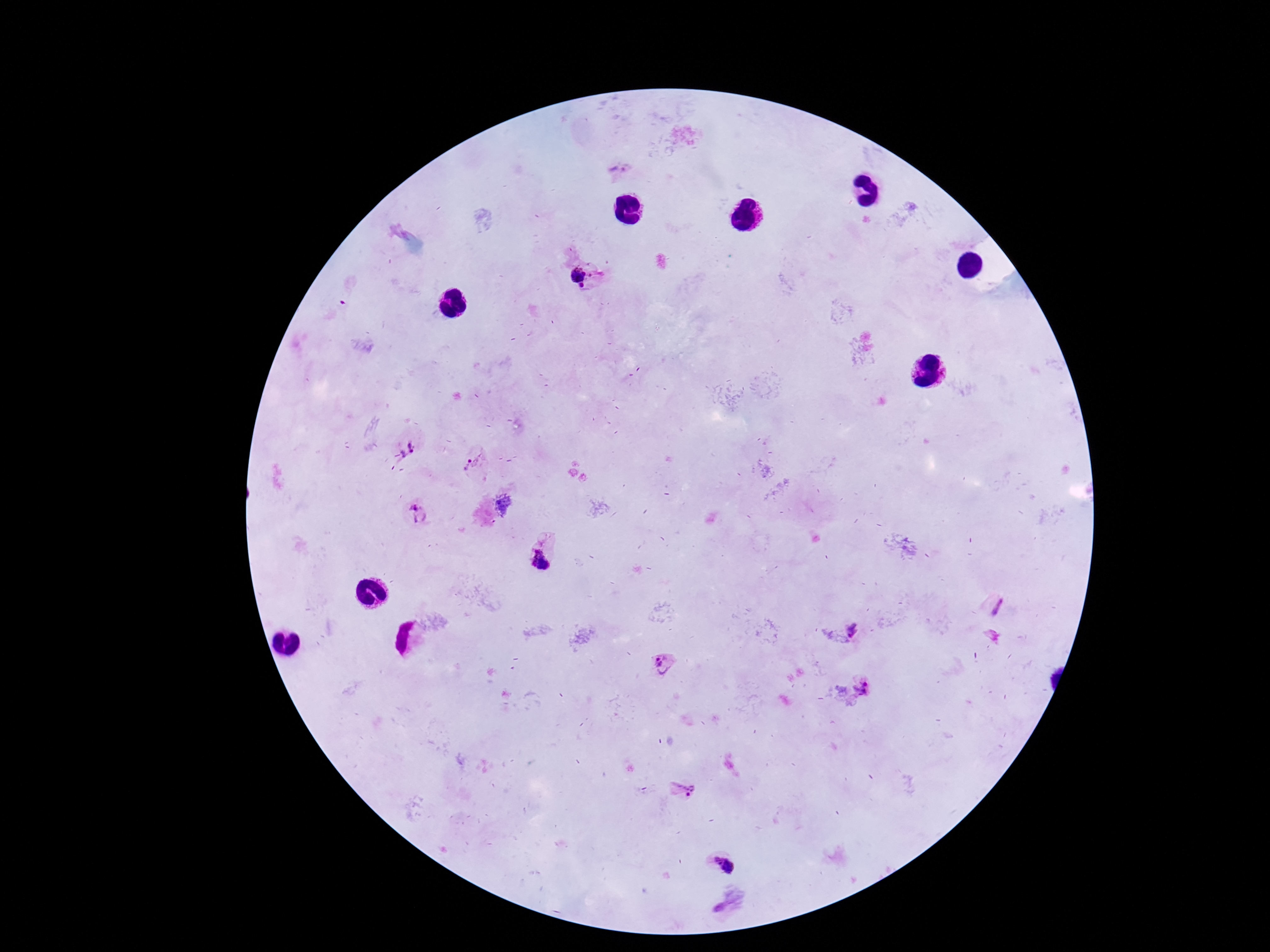

Plasmodium parasite locations = approximate centers as {x, y} in pixels: {619, 171}, {581, 277}, {407, 450}, {473, 462}, {416, 513}, {540, 560}, {998, 606}, {853, 629}, {666, 665}, {863, 687}, {683, 790}, {721, 864}
image size = 1270×952 pixels
stain = Giemsa
capture = smartphone camera through the microscope eyepiece
preparation = thick blood smear
magnification = 100x
field of view = single
patient malaria status = infected